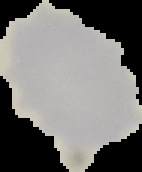

Summary:
  - Preparation: thin blood smear
  - Malaria status: uninfected
  - Image type: segmented cell region on a black background
  - Image size: 142×172 pixels